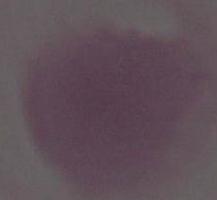
Summary:
  - Identification: erythrocyte
  - Modality: photomicrograph
  - Magnification: 1000x